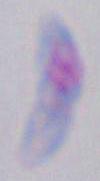
{
  "magnification": "1000x",
  "modality": "micrograph",
  "identification": "Toxoplasma gondii"
}